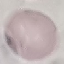 Malaria status: uninfected. Automatically extracted cell patch, resized to 64 × 64 pixels. Thin blood film. Acquired by smartphone through the microscope eyepiece. Giemsa-stained preparation.